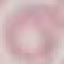
result = no malaria parasites seen
preparation = thin blood film
capture = smartphone camera at the microscope eyepiece
image type = cell patch, automatically extracted from a larger field of view and resized to 64 × 64 pixels
stain = Giemsa